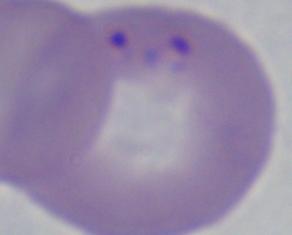
identification = Babesia
magnification = 1000x
modality = photomicrograph